Classify this cell by malaria status.
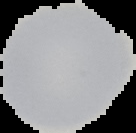
Uninfected.

Summary:
  - Image size: 136×133 pixels
  - Image type: cell region segmented out of the field of view; surrounding area masked to black
  - Preparation: thin blood smear